Assess this cell for malaria.
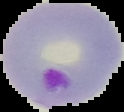
It is parasitized.

Image is 124×112 pixels. Segmented cell region on a black background. From a thin blood film.